State which cell type is depicted.
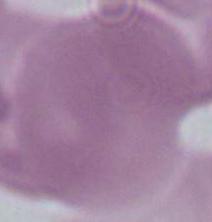

An erythrocyte.

modality = micrograph
magnification = 1000x